Locate every P. falciparum parasite and identify its life-cycle stage.
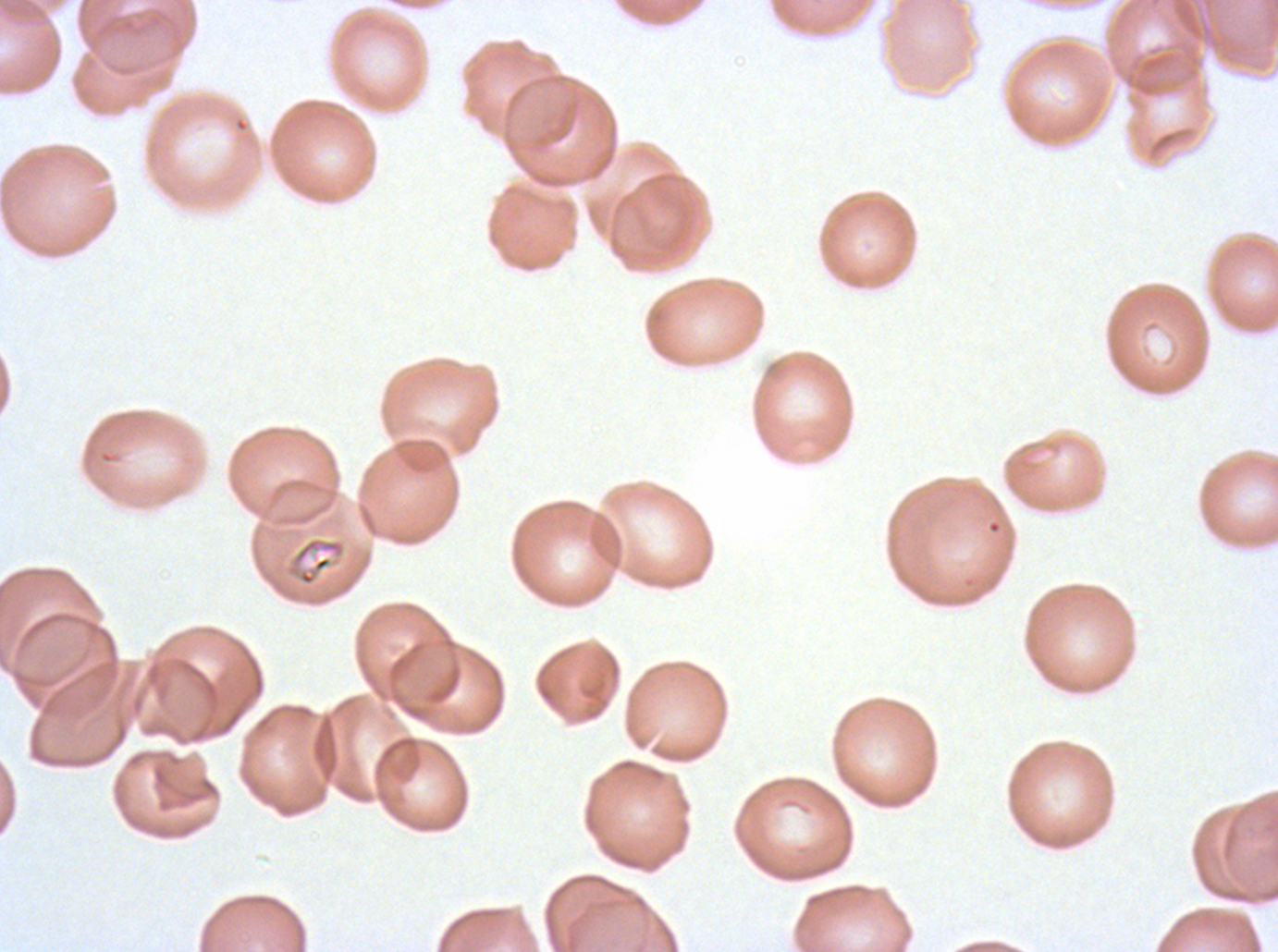
No rings, late-ring/early-trophozoite forms, mid trophozoites, late trophozoites, early schizonts, late schizonts, segmenters, or gametocytes observed.

Approximate bounding boxes as (x1, y1, x2, y2) in pixels.
Summary:
  - Debris locations: (284, 536, 347, 587)
  - Specimen: ex-vivo P. falciparum culture from a patient in The Gambia, grown for 24 to 48 hours
  - Preparation: thin blood film
  - Stain: Giemsa
  - Image size: 1278×952 pixels
  - Field of view: one sub-image of a larger composite